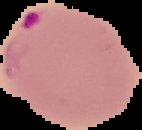
image size = 142×130 pixels
preparation = thin blood film
result = malaria parasites identified
image type = segmented cell region on a black background